Name the parasite shown.
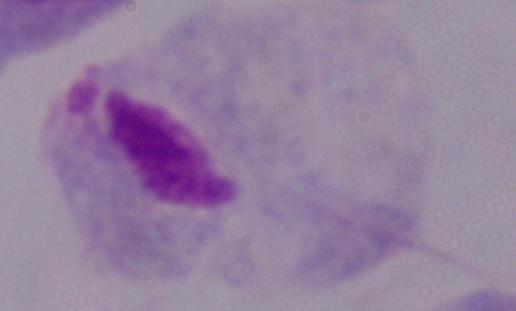
This is a trichomonad.

Photomicrograph. Captured at 1000x magnification.